Assess this cell for malaria.
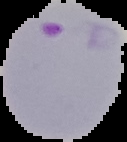

Parasitized.

Summary:
  - Image size: 127×142 pixels
  - Preparation: thin blood smear
  - Image type: segmented cell region on a black background